Locate every uninfected red blood cell.
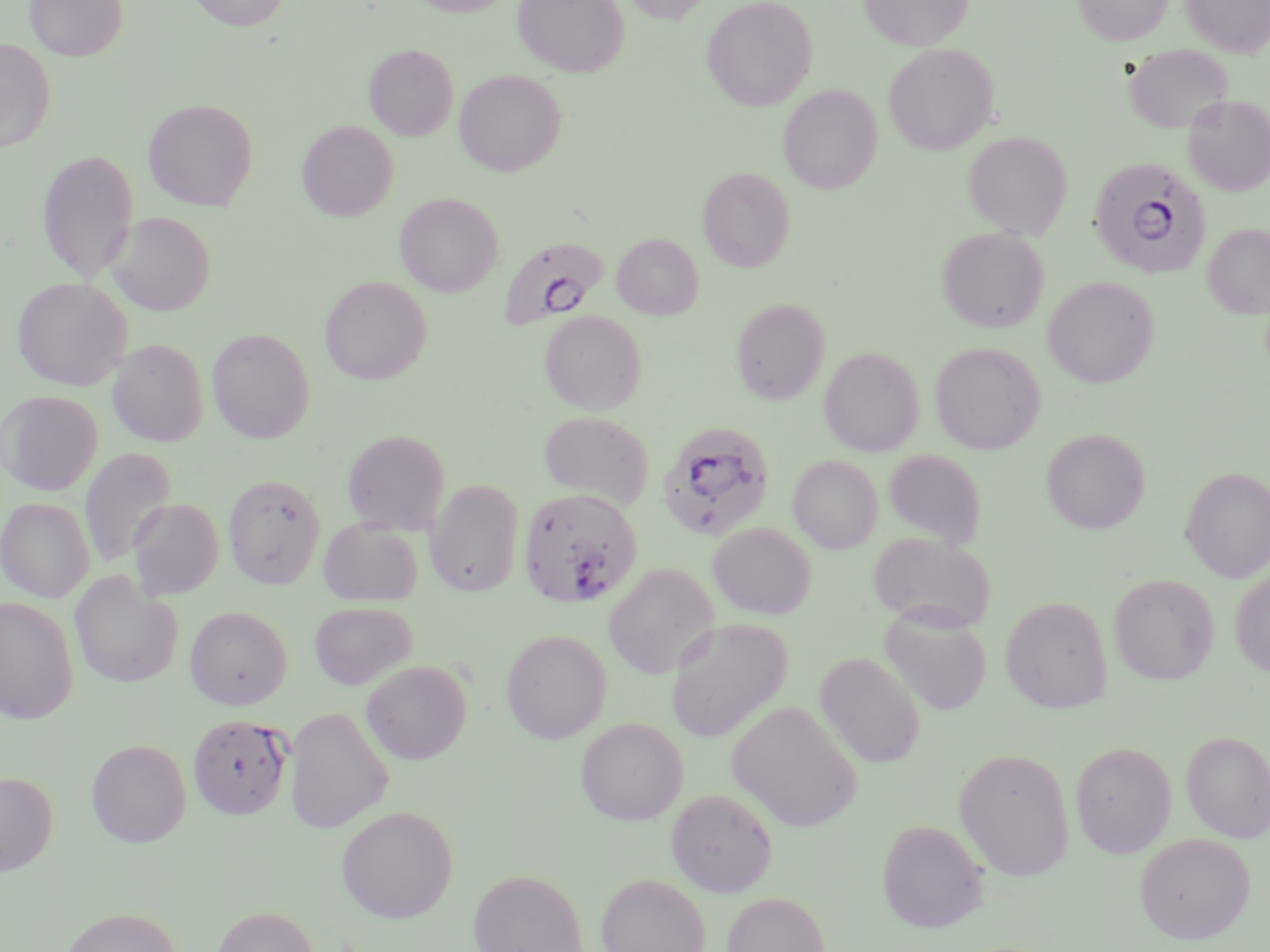
Approximate bounding boxes as named x1/y1/x2/y2 corners in pixels.
Uninfected red blood cells: (x1=25, y1=0, x2=128, y2=61), (x1=189, y1=0, x2=291, y2=31), (x1=406, y1=0, x2=516, y2=16), (x1=512, y1=0, x2=630, y2=77), (x1=620, y1=0, x2=716, y2=25), (x1=701, y1=0, x2=818, y2=111), (x1=859, y1=0, x2=972, y2=51), (x1=1072, y1=0, x2=1173, y2=45), (x1=1181, y1=0, x2=1270, y2=57), (x1=0, y1=39, x2=56, y2=152), (x1=364, y1=43, x2=458, y2=140), (x1=883, y1=43, x2=997, y2=155), (x1=1123, y1=44, x2=1234, y2=134), (x1=454, y1=69, x2=567, y2=176), (x1=778, y1=85, x2=883, y2=194), (x1=1182, y1=95, x2=1270, y2=196), (x1=143, y1=98, x2=259, y2=211), (x1=298, y1=121, x2=398, y2=220), (x1=963, y1=131, x2=1072, y2=239), (x1=37, y1=149, x2=140, y2=284), (x1=698, y1=166, x2=795, y2=272), (x1=395, y1=192, x2=503, y2=296), (x1=106, y1=211, x2=216, y2=316), (x1=1203, y1=223, x2=1270, y2=319), (x1=936, y1=227, x2=1048, y2=332), (x1=612, y1=233, x2=703, y2=319), (x1=320, y1=275, x2=432, y2=385), (x1=13, y1=276, x2=132, y2=390), (x1=1042, y1=276, x2=1159, y2=388), (x1=731, y1=298, x2=830, y2=404), (x1=540, y1=310, x2=647, y2=415), (x1=208, y1=328, x2=315, y2=443), (x1=108, y1=339, x2=208, y2=446), (x1=930, y1=342, x2=1044, y2=454), (x1=819, y1=346, x2=924, y2=456), (x1=0, y1=391, x2=102, y2=496), (x1=538, y1=410, x2=654, y2=510), (x1=1042, y1=428, x2=1149, y2=534), (x1=342, y1=429, x2=451, y2=534), (x1=79, y1=446, x2=176, y2=569), (x1=882, y1=449, x2=987, y2=549), (x1=789, y1=455, x2=883, y2=553), (x1=1181, y1=466, x2=1270, y2=582), (x1=223, y1=473, x2=325, y2=588), (x1=426, y1=479, x2=524, y2=597), (x1=0, y1=498, x2=95, y2=603), (x1=128, y1=498, x2=223, y2=599), (x1=319, y1=518, x2=424, y2=607), (x1=708, y1=522, x2=816, y2=619), (x1=868, y1=531, x2=996, y2=632), (x1=604, y1=563, x2=719, y2=679), (x1=1230, y1=569, x2=1270, y2=677), (x1=70, y1=572, x2=183, y2=689), (x1=1109, y1=573, x2=1219, y2=685), (x1=1000, y1=596, x2=1113, y2=713), (x1=0, y1=597, x2=79, y2=723), (x1=309, y1=601, x2=417, y2=690), (x1=185, y1=606, x2=291, y2=709), (x1=880, y1=608, x2=992, y2=715), (x1=666, y1=619, x2=792, y2=742), (x1=501, y1=629, x2=612, y2=743), (x1=814, y1=652, x2=926, y2=768), (x1=362, y1=660, x2=472, y2=764), (x1=727, y1=701, x2=862, y2=831), (x1=285, y1=707, x2=393, y2=833), (x1=575, y1=717, x2=688, y2=825), (x1=1181, y1=730, x2=1270, y2=842), (x1=87, y1=739, x2=191, y2=847), (x1=1070, y1=741, x2=1176, y2=858), (x1=954, y1=747, x2=1075, y2=881), (x1=0, y1=771, x2=57, y2=876), (x1=667, y1=788, x2=778, y2=896), (x1=336, y1=805, x2=458, y2=922), (x1=876, y1=819, x2=989, y2=932), (x1=1134, y1=832, x2=1255, y2=943), (x1=468, y1=868, x2=589, y2=952), (x1=596, y1=872, x2=711, y2=952), (x1=722, y1=891, x2=830, y2=952), (x1=212, y1=905, x2=319, y2=952), (x1=60, y1=906, x2=182, y2=952).

{
  "slide_level_diagnosis": "Plasmodium falciparum",
  "modality": "light microscopy",
  "field_of_view": "one of a larger specimen",
  "preparation": "thin blood smear",
  "plasmodium_falciparum_infected_red_blood_cell_locations": "approximate bounding boxes as named x1/y1/x2/y2 corners in pixels: (x1=1087, y1=154, x2=1212, y2=278), (x1=500, y1=238, x2=602, y2=329), (x1=656, y1=421, x2=776, y2=541), (x1=519, y1=488, x2=642, y2=608), (x1=187, y1=714, x2=292, y2=820)",
  "image_size": "1270×952 pixels",
  "magnification": "1000x",
  "stain": "May-Grünwald-Giemsa"
}